Describe the morphology of the red blood cells.
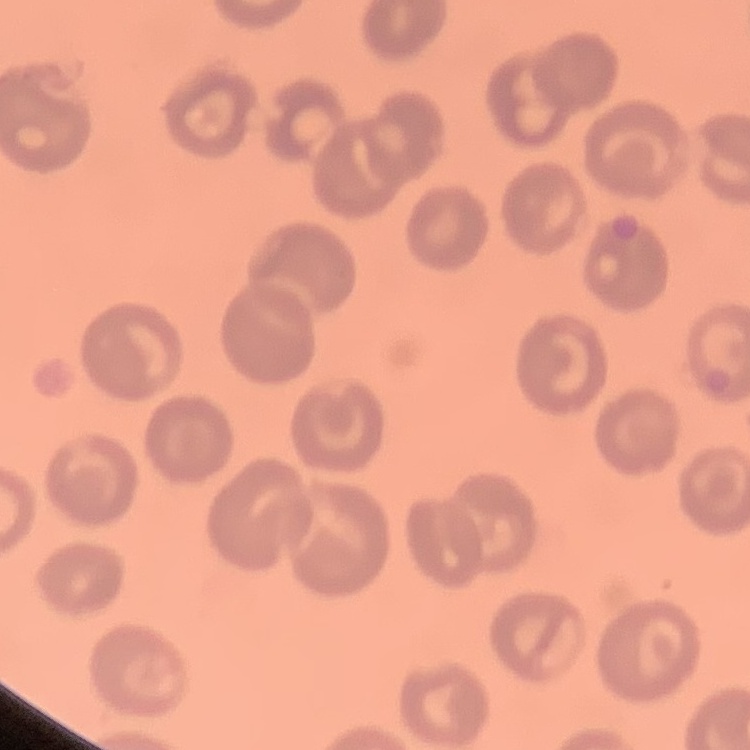

They show no rouleaux formation.

Summary:
  - Stain: Field's or Giemsa
  - Image type: one tile cut from a larger photomicrograph
  - Preparation: thin peripheral smear